State the blood parasite species.
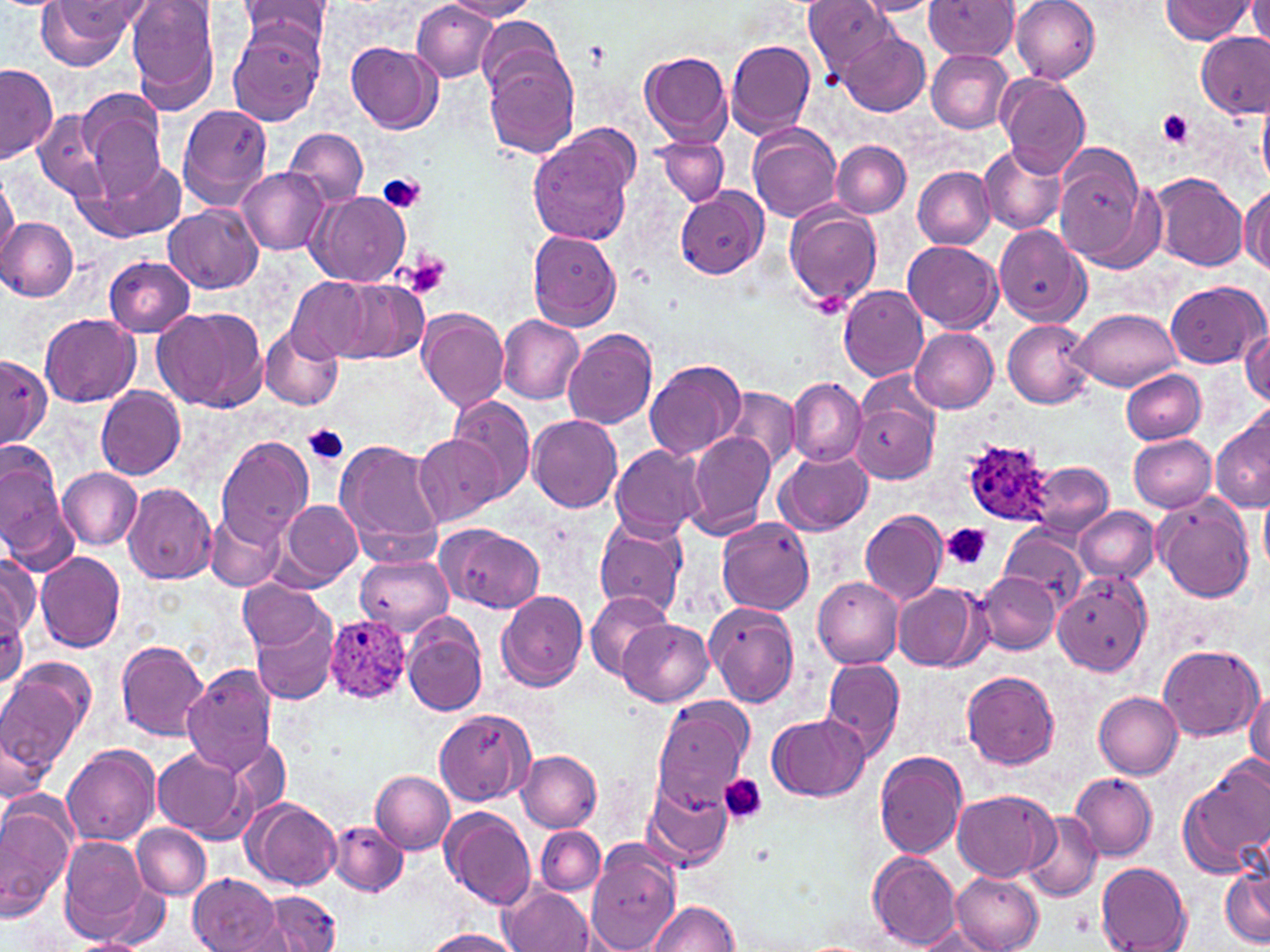

Plasmodium ovale.

image size = 1270×952 pixels
magnification = 1000x
platelet locations = approximate bounding boxes as named x1/y1/x2/y2 corners in pixels: (x1=1156, y1=109, x2=1197, y2=150), (x1=377, y1=174, x2=426, y2=215), (x1=405, y1=254, x2=451, y2=299), (x1=304, y1=425, x2=349, y2=465), (x1=943, y1=522, x2=991, y2=570), (x1=721, y1=774, x2=766, y2=824)
field of view = single
Plasmodium ovale-infected red blood cell locations = approximate bounding boxes as named x1/y1/x2/y2 corners in pixels: (x1=961, y1=439, x2=1051, y2=524), (x1=324, y1=616, x2=410, y2=702)
preparation = thin blood smear
uninfected red blood cell locations = approximate bounding boxes as named x1/y1/x2/y2 corners in pixels: (x1=36, y1=0, x2=137, y2=70), (x1=126, y1=0, x2=220, y2=111), (x1=238, y1=0, x2=332, y2=56), (x1=804, y1=0, x2=898, y2=80), (x1=924, y1=0, x2=1019, y2=61), (x1=1010, y1=0, x2=1099, y2=84), (x1=1248, y1=0, x2=1269, y2=52), (x1=442, y1=1, x2=539, y2=21), (x1=854, y1=1, x2=943, y2=16), (x1=1161, y1=1, x2=1255, y2=44), (x1=413, y1=2, x2=497, y2=82), (x1=477, y1=15, x2=566, y2=100), (x1=229, y1=20, x2=325, y2=126), (x1=839, y1=27, x2=931, y2=116), (x1=1197, y1=31, x2=1268, y2=118), (x1=725, y1=38, x2=816, y2=139), (x1=346, y1=42, x2=441, y2=133), (x1=927, y1=48, x2=1014, y2=134), (x1=639, y1=49, x2=734, y2=146), (x1=485, y1=58, x2=578, y2=159), (x1=0, y1=65, x2=58, y2=164), (x1=995, y1=71, x2=1090, y2=177), (x1=75, y1=90, x2=166, y2=195), (x1=1258, y1=98, x2=1270, y2=187), (x1=176, y1=104, x2=274, y2=209), (x1=37, y1=112, x2=111, y2=198), (x1=748, y1=124, x2=843, y2=221), (x1=527, y1=125, x2=639, y2=247), (x1=285, y1=127, x2=370, y2=209), (x1=656, y1=136, x2=729, y2=206), (x1=831, y1=140, x2=910, y2=217), (x1=979, y1=143, x2=1066, y2=235), (x1=1050, y1=150, x2=1156, y2=270), (x1=75, y1=157, x2=186, y2=244), (x1=236, y1=167, x2=329, y2=254), (x1=913, y1=167, x2=995, y2=248), (x1=1149, y1=173, x2=1246, y2=272), (x1=0, y1=174, x2=18, y2=265), (x1=1239, y1=185, x2=1270, y2=275), (x1=676, y1=188, x2=768, y2=279), (x1=307, y1=191, x2=410, y2=287), (x1=785, y1=201, x2=882, y2=311), (x1=165, y1=205, x2=262, y2=292), (x1=1, y1=218, x2=78, y2=301), (x1=993, y1=225, x2=1091, y2=327), (x1=527, y1=230, x2=622, y2=331), (x1=901, y1=242, x2=1000, y2=330), (x1=105, y1=256, x2=196, y2=336), (x1=285, y1=275, x2=390, y2=363), (x1=1167, y1=281, x2=1265, y2=368), (x1=838, y1=286, x2=927, y2=381), (x1=154, y1=306, x2=268, y2=415), (x1=417, y1=308, x2=510, y2=412), (x1=1072, y1=309, x2=1181, y2=391), (x1=41, y1=313, x2=139, y2=407), (x1=497, y1=315, x2=584, y2=403), (x1=1002, y1=319, x2=1094, y2=408), (x1=1241, y1=326, x2=1270, y2=406), (x1=260, y1=328, x2=343, y2=409), (x1=563, y1=328, x2=658, y2=430), (x1=911, y1=328, x2=999, y2=413), (x1=0, y1=357, x2=52, y2=445), (x1=644, y1=358, x2=746, y2=461), (x1=1122, y1=368, x2=1206, y2=445), (x1=789, y1=376, x2=865, y2=467), (x1=723, y1=384, x2=800, y2=472), (x1=94, y1=385, x2=186, y2=479), (x1=849, y1=394, x2=940, y2=485), (x1=449, y1=396, x2=535, y2=500), (x1=1212, y1=408, x2=1270, y2=513), (x1=528, y1=415, x2=623, y2=513), (x1=683, y1=430, x2=776, y2=538), (x1=1128, y1=433, x2=1215, y2=512), (x1=414, y1=434, x2=504, y2=525), (x1=215, y1=437, x2=314, y2=546), (x1=333, y1=439, x2=445, y2=558), (x1=0, y1=443, x2=72, y2=568), (x1=610, y1=444, x2=705, y2=539), (x1=777, y1=449, x2=873, y2=536), (x1=1026, y1=462, x2=1112, y2=539), (x1=58, y1=467, x2=142, y2=549), (x1=122, y1=484, x2=216, y2=583), (x1=1259, y1=491, x2=1270, y2=574), (x1=1154, y1=495, x2=1255, y2=603), (x1=279, y1=500, x2=363, y2=586), (x1=1075, y1=506, x2=1158, y2=584), (x1=860, y1=510, x2=946, y2=604), (x1=204, y1=511, x2=286, y2=592), (x1=594, y1=515, x2=688, y2=616), (x1=715, y1=517, x2=816, y2=615), (x1=435, y1=523, x2=545, y2=613), (x1=1000, y1=525, x2=1087, y2=612), (x1=35, y1=551, x2=127, y2=654), (x1=2, y1=552, x2=37, y2=643), (x1=355, y1=552, x2=454, y2=635), (x1=974, y1=570, x2=1061, y2=656), (x1=1053, y1=572, x2=1152, y2=677), (x1=814, y1=577, x2=903, y2=670), (x1=238, y1=578, x2=329, y2=653), (x1=893, y1=583, x2=986, y2=670), (x1=496, y1=590, x2=589, y2=692), (x1=584, y1=591, x2=674, y2=680), (x1=705, y1=602, x2=800, y2=708), (x1=252, y1=609, x2=341, y2=705), (x1=402, y1=613, x2=488, y2=713), (x1=618, y1=618, x2=714, y2=705), (x1=114, y1=641, x2=212, y2=741), (x1=1157, y1=646, x2=1263, y2=742), (x1=0, y1=657, x2=95, y2=775), (x1=821, y1=657, x2=907, y2=762), (x1=183, y1=665, x2=280, y2=776), (x1=962, y1=670, x2=1059, y2=769), (x1=1245, y1=688, x2=1270, y2=772), (x1=1094, y1=691, x2=1184, y2=779), (x1=650, y1=696, x2=754, y2=809), (x1=435, y1=708, x2=537, y2=805), (x1=768, y1=713, x2=869, y2=801), (x1=2, y1=723, x2=53, y2=806), (x1=62, y1=743, x2=160, y2=845), (x1=152, y1=748, x2=246, y2=841), (x1=517, y1=749, x2=603, y2=831), (x1=875, y1=749, x2=968, y2=859), (x1=1179, y1=760, x2=1270, y2=879), (x1=372, y1=770, x2=455, y2=855), (x1=1071, y1=772, x2=1157, y2=862), (x1=644, y1=778, x2=734, y2=870), (x1=952, y1=789, x2=1059, y2=882), (x1=246, y1=798, x2=343, y2=892), (x1=0, y1=803, x2=74, y2=920), (x1=441, y1=806, x2=535, y2=908), (x1=1022, y1=812, x2=1103, y2=903), (x1=329, y1=819, x2=408, y2=896), (x1=131, y1=823, x2=212, y2=899), (x1=535, y1=827, x2=605, y2=896), (x1=60, y1=835, x2=154, y2=944), (x1=585, y1=842, x2=682, y2=952), (x1=869, y1=850, x2=962, y2=949), (x1=1221, y1=862, x2=1270, y2=949), (x1=1096, y1=863, x2=1191, y2=951), (x1=950, y1=871, x2=1044, y2=952), (x1=188, y1=873, x2=284, y2=951), (x1=502, y1=885, x2=593, y2=952), (x1=261, y1=891, x2=341, y2=952), (x1=648, y1=898, x2=740, y2=951), (x1=913, y1=925, x2=996, y2=950), (x1=419, y1=929, x2=521, y2=952), (x1=69, y1=937, x2=151, y2=952)
modality = light microscopy
stain = May-Grünwald-Giemsa